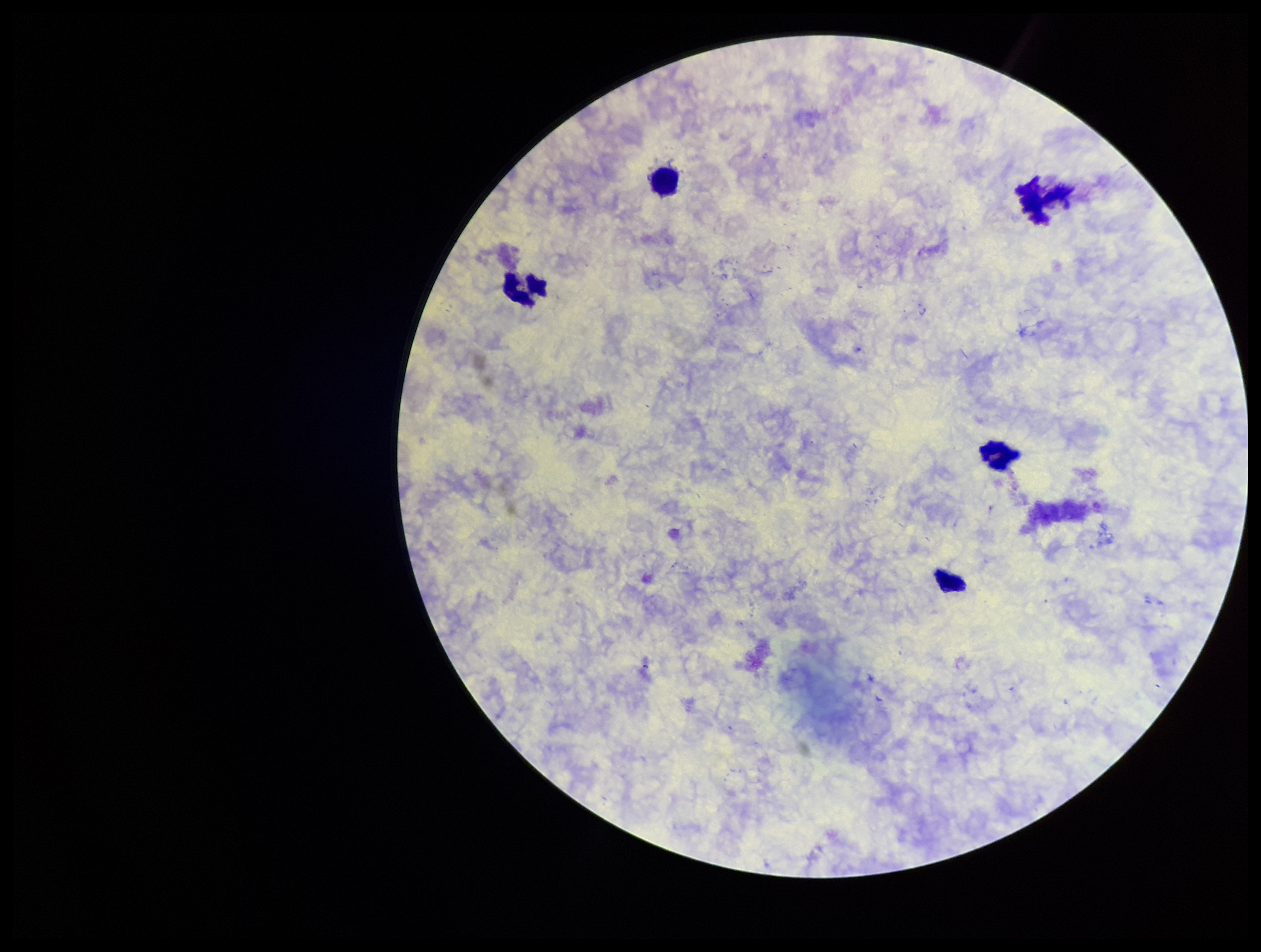
{
  "capture": "smartphone photograph through the microscope eyepiece",
  "patient_malaria_status": "negative",
  "field_of_view": "one from this slide",
  "stain": "Giemsa",
  "plasmodium_parasites": "none detected",
  "leukocyte_count": 4,
  "parasite_count": 0,
  "image_size": "1261×952 pixels",
  "preparation": "thick blood smear"
}